Report the malaria status of this cell.
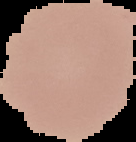

It is uninfected.

Summary:
  - Image type: segmented cell region on a black background
  - Preparation: thin blood film
  - Image size: 136×142 pixels